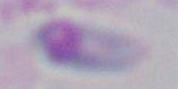
Toxoplasma gondii is shown. Captured at 1000x magnification. Photomicrograph.